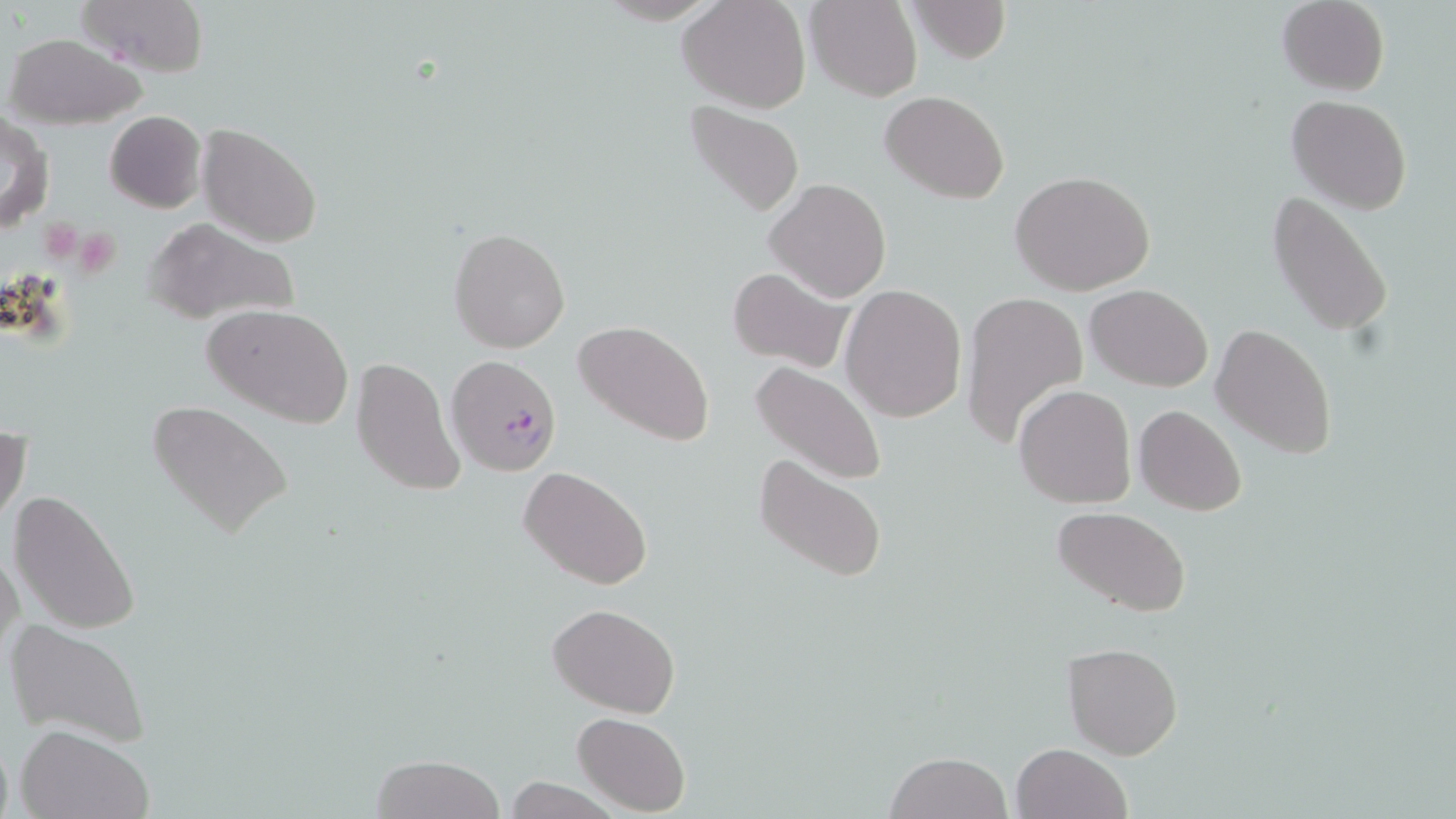

slide-level diagnosis = Plasmodium falciparum
platelet locations = approximate bounding boxes as named x1/y1/x2/y2 corners in pixels: (x1=73, y1=230, x2=122, y2=277)
stain = May-Grünwald-Giemsa
modality = light microscopy
preparation = thin blood smear
field of view = single
image size = 1456×819 pixels
uninfected red blood cell locations = approximate bounding boxes as named x1/y1/x2/y2 corners in pixels: (x1=76, y1=0, x2=209, y2=78), (x1=678, y1=0, x2=811, y2=113), (x1=910, y1=0, x2=1015, y2=65), (x1=1277, y1=0, x2=1389, y2=95), (x1=807, y1=1, x2=922, y2=101), (x1=5, y1=33, x2=149, y2=128), (x1=882, y1=91, x2=1009, y2=204), (x1=1287, y1=94, x2=1412, y2=214), (x1=683, y1=101, x2=804, y2=219), (x1=104, y1=110, x2=206, y2=212), (x1=1, y1=113, x2=55, y2=232), (x1=198, y1=123, x2=323, y2=249), (x1=1010, y1=169, x2=1157, y2=296), (x1=765, y1=179, x2=891, y2=300), (x1=1267, y1=187, x2=1396, y2=340), (x1=142, y1=218, x2=303, y2=329), (x1=448, y1=226, x2=571, y2=354), (x1=727, y1=266, x2=854, y2=373), (x1=841, y1=283, x2=967, y2=421), (x1=1085, y1=283, x2=1212, y2=391), (x1=959, y1=291, x2=1088, y2=448), (x1=204, y1=304, x2=355, y2=430), (x1=573, y1=318, x2=716, y2=448), (x1=1211, y1=324, x2=1338, y2=459), (x1=351, y1=355, x2=467, y2=497), (x1=750, y1=359, x2=889, y2=487), (x1=1014, y1=384, x2=1136, y2=508), (x1=148, y1=398, x2=294, y2=542), (x1=1135, y1=405, x2=1248, y2=515), (x1=0, y1=427, x2=30, y2=527), (x1=752, y1=451, x2=889, y2=584), (x1=519, y1=464, x2=655, y2=590), (x1=8, y1=490, x2=143, y2=636), (x1=1050, y1=504, x2=1193, y2=617), (x1=1, y1=544, x2=25, y2=671), (x1=546, y1=603, x2=681, y2=717), (x1=5, y1=616, x2=153, y2=748), (x1=1062, y1=642, x2=1183, y2=760), (x1=573, y1=712, x2=690, y2=816), (x1=15, y1=725, x2=152, y2=819), (x1=1011, y1=743, x2=1131, y2=819), (x1=884, y1=751, x2=1013, y2=819), (x1=370, y1=753, x2=505, y2=819), (x1=501, y1=778, x2=622, y2=817)
Plasmodium falciparum-infected red blood cell locations = approximate bounding boxes as named x1/y1/x2/y2 corners in pixels: (x1=448, y1=355, x2=562, y2=477)
magnification = 1000x